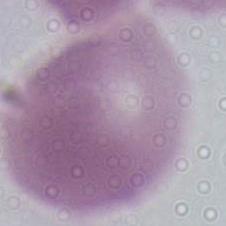 An erythrocyte is seen. Photomicrograph. 1000x magnification.